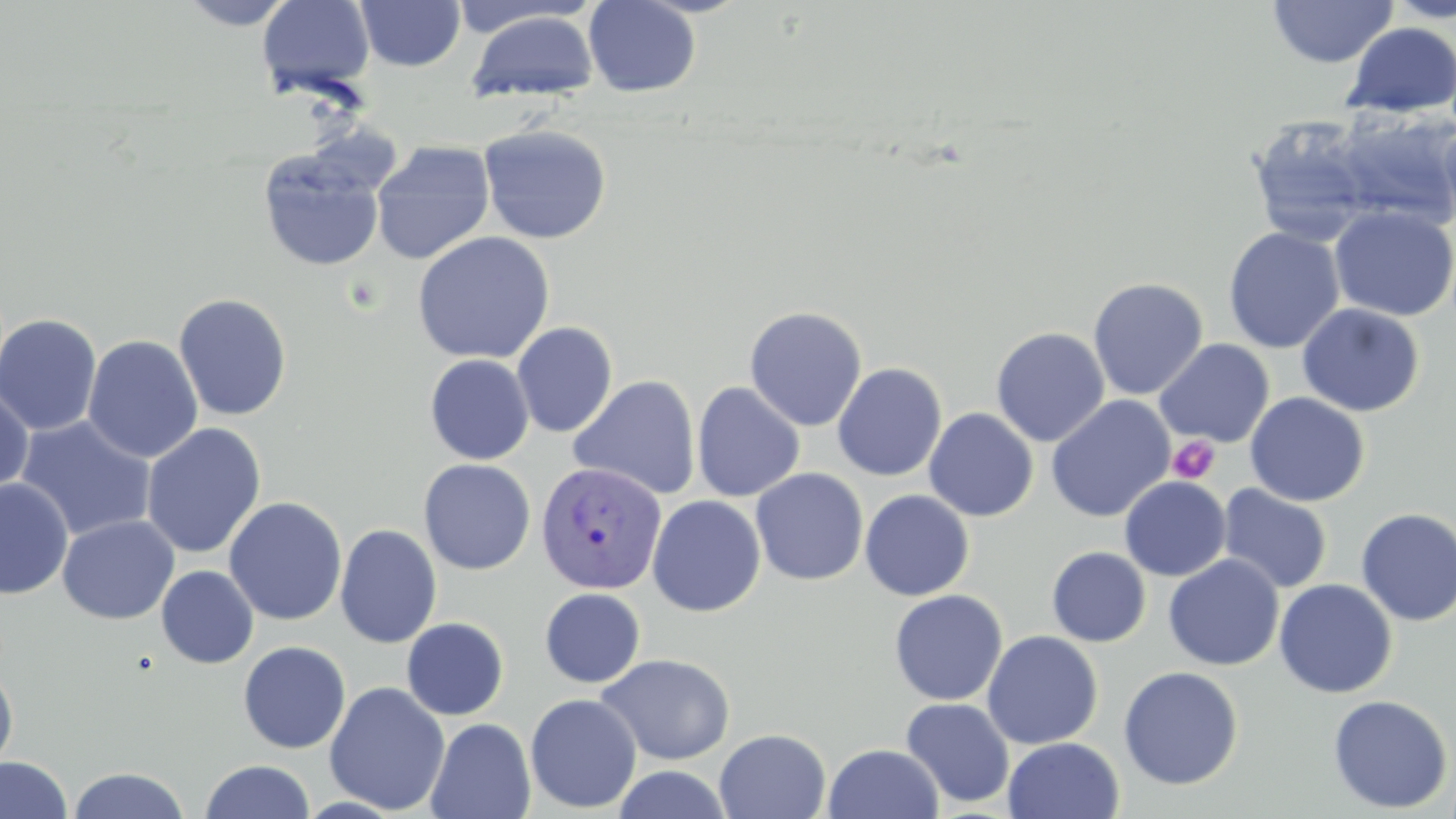

Summary:
  - Coordinate format: approximate bounding boxes as [x1, y1, x2, y2] in pixels
  - Uninfected red blood cell locations: [174, 0, 300, 30], [256, 0, 376, 98], [355, 0, 465, 71], [583, 0, 701, 97], [1382, 0, 1456, 23], [1267, 1, 1399, 68], [444, 2, 601, 39], [465, 10, 600, 104], [1341, 21, 1456, 118], [1327, 108, 1456, 233], [1247, 116, 1378, 246], [1439, 118, 1456, 234], [477, 124, 613, 244], [371, 141, 496, 265], [257, 148, 386, 272], [1329, 206, 1456, 322], [1223, 227, 1345, 354], [412, 231, 555, 364], [1088, 277, 1208, 400], [173, 293, 293, 421], [1297, 303, 1425, 417], [744, 305, 868, 432], [0, 313, 102, 436], [512, 321, 618, 437], [991, 327, 1110, 447], [82, 335, 204, 464], [1154, 338, 1275, 447], [424, 354, 534, 465], [832, 361, 947, 481], [569, 375, 701, 500], [691, 381, 806, 502], [0, 383, 34, 498], [1245, 392, 1370, 506], [1046, 395, 1175, 523], [924, 407, 1039, 521], [15, 415, 157, 542], [140, 422, 266, 559], [418, 458, 536, 575], [751, 468, 869, 586], [1119, 476, 1231, 581], [0, 478, 73, 599], [1217, 484, 1333, 594], [859, 490, 974, 601], [647, 495, 766, 617], [224, 496, 347, 625], [1355, 508, 1456, 627], [57, 514, 180, 625], [334, 523, 442, 649], [1046, 546, 1151, 647], [1163, 554, 1284, 670], [156, 565, 259, 669], [1273, 579, 1398, 698], [539, 588, 646, 688], [890, 589, 1008, 705], [401, 617, 509, 720], [982, 630, 1103, 749], [238, 641, 351, 754], [596, 653, 736, 765], [0, 662, 18, 777], [1118, 665, 1243, 790], [324, 681, 450, 815], [525, 694, 643, 813], [1328, 695, 1453, 814], [900, 697, 1015, 808], [425, 717, 536, 819], [714, 729, 831, 819], [1002, 736, 1124, 819], [822, 743, 944, 819], [0, 756, 72, 818], [199, 759, 316, 818], [611, 765, 733, 819], [67, 766, 192, 818]
  - Platelet locations: [1167, 436, 1220, 484]
  - Plasmodium vivax-infected red blood cell locations: [535, 461, 668, 593]
  - Slide-level diagnosis: Plasmodium vivax
  - Field of view: single
  - Modality: light microscopy
  - Image size: 1456×819 pixels
  - Magnification: 1000x
  - Stain: May-Grünwald-Giemsa
  - Preparation: thin blood film